Name the parasite shown.
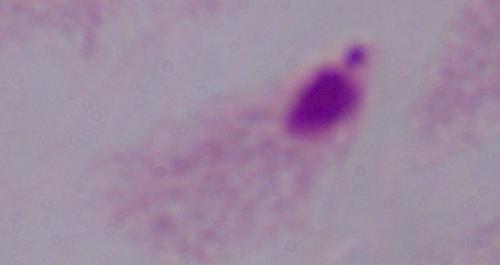
This is a trichomonad.

Micrograph. 1000x magnification.